State the preparation type.
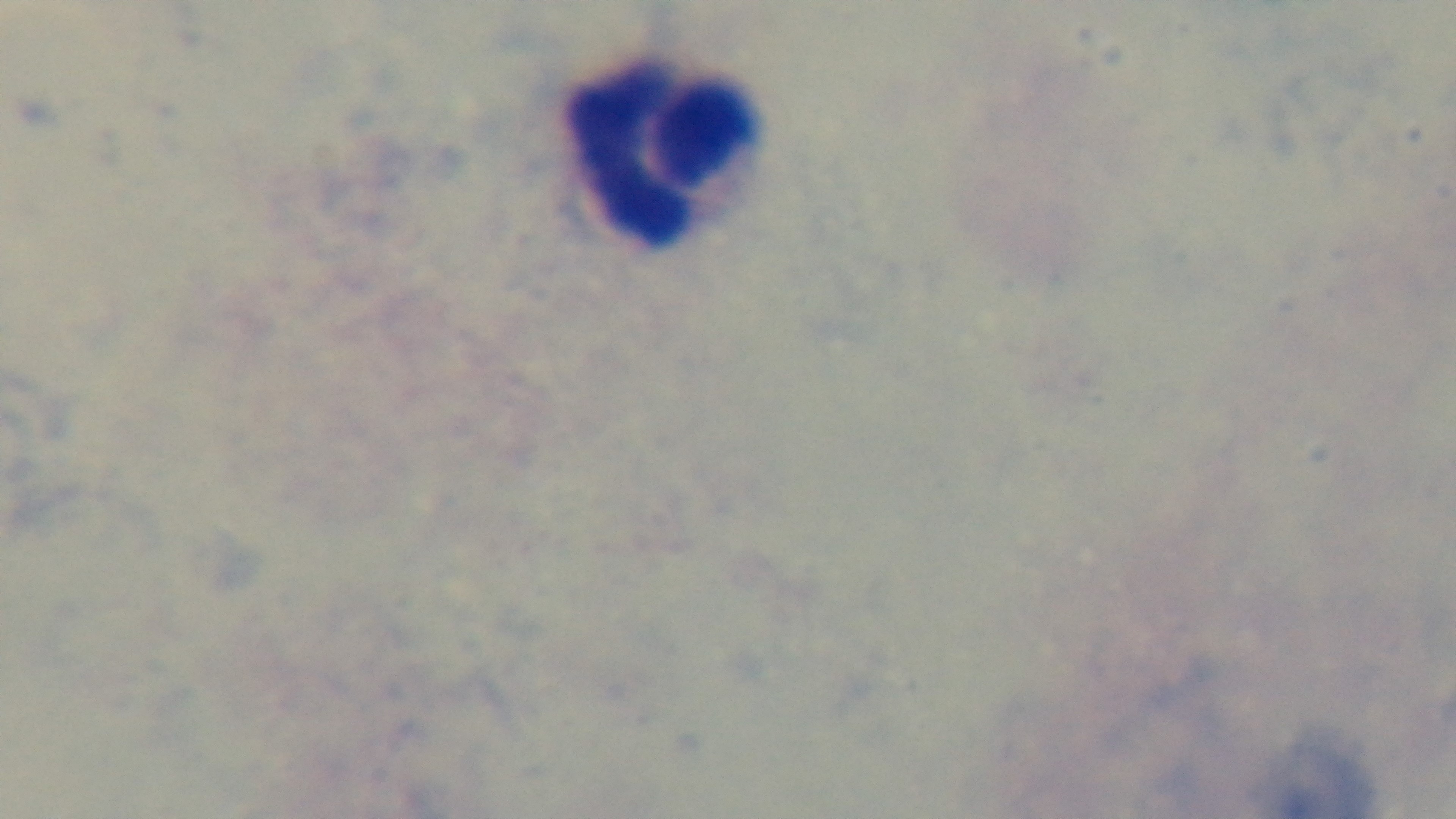

Thick.

{
  "field_of_view": "single",
  "modality": "light microscopy",
  "stain": "Giemsa",
  "objective": "100x oil immersion",
  "malaria_status": "uninfected",
  "capture": "mounted 4K digital camera"
}